Name the parasite shown.
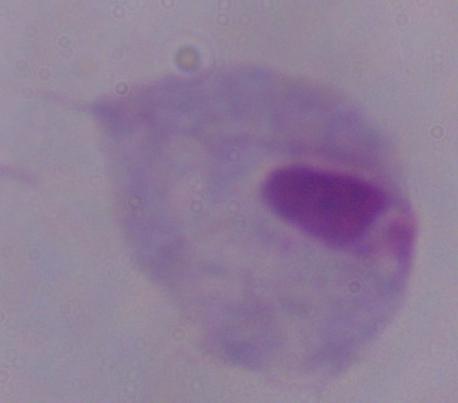

A trichomonad.

magnification: 1000x
modality: micrograph